Assess the morphology of the erythrocytes.
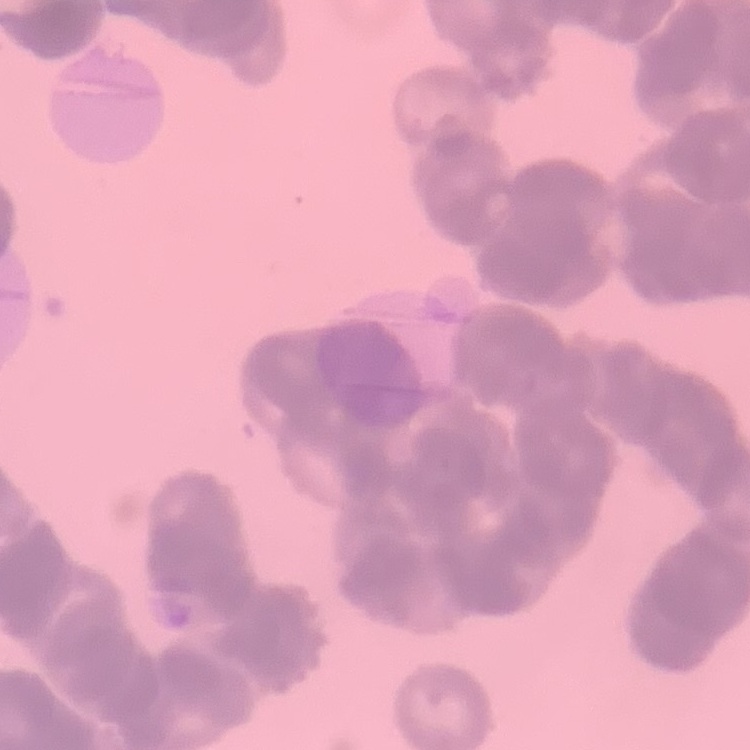
They show rouleaux formation.

Summary:
  - Stain: Field's or Giemsa
  - Image type: square crop of a larger photomicrograph
  - Preparation: thin blood film